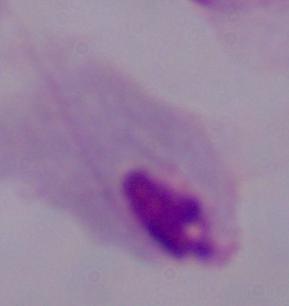 Captured at 1000x magnification. A trichomonad is seen. Photomicrograph.